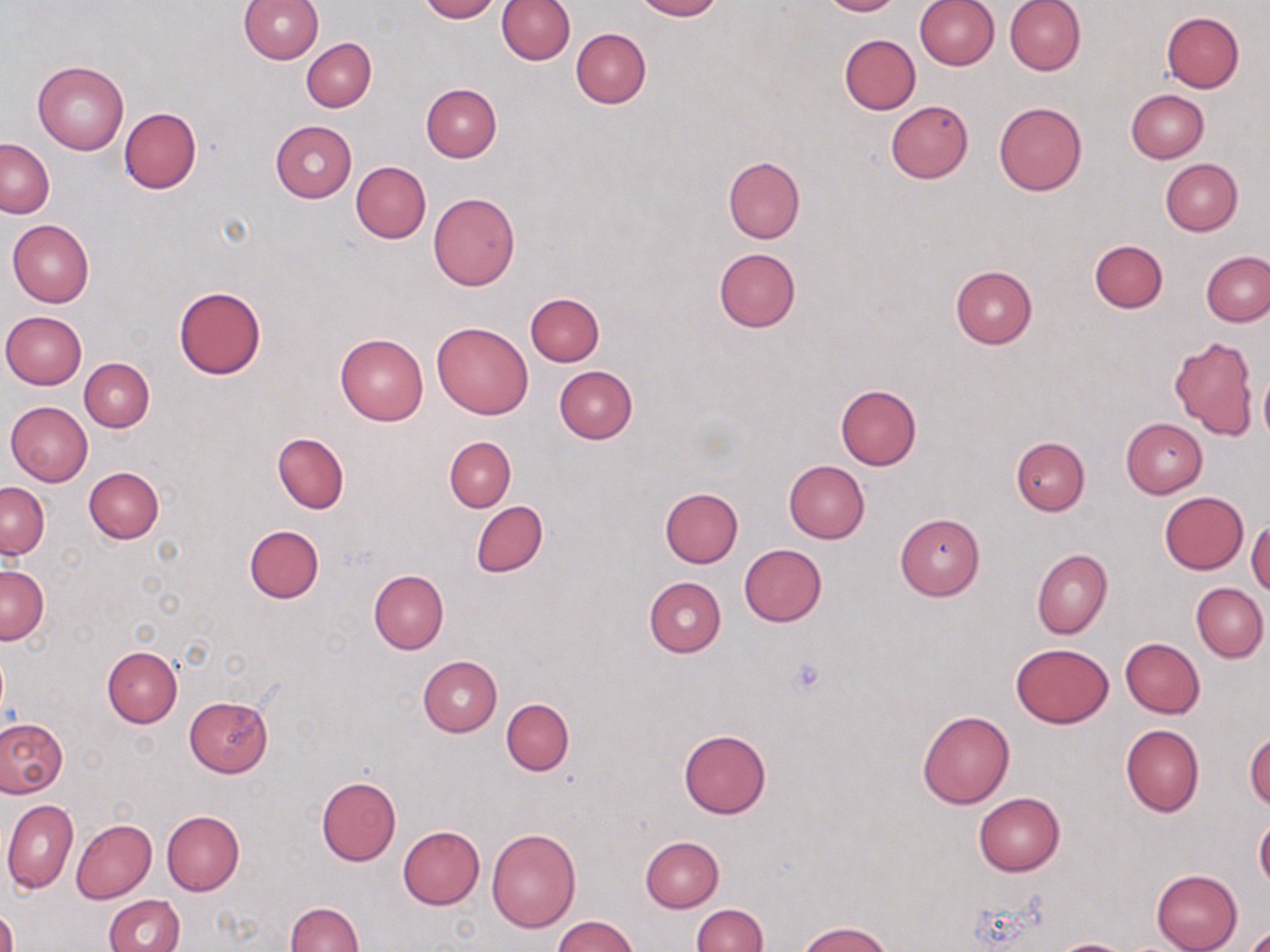
Approximate bounding boxes as (x1, y1, x2, y2) in pixels. Platelet locations: (786, 656, 830, 700). Uninfected red blood cell locations: (239, 0, 323, 63), (419, 0, 501, 22), (496, 0, 575, 65), (630, 0, 721, 20), (820, 0, 901, 15), (914, 0, 999, 71), (1005, 0, 1085, 75), (1162, 12, 1244, 92), (571, 28, 651, 108), (839, 34, 920, 114), (302, 38, 376, 112), (33, 60, 129, 154), (422, 84, 502, 162), (1126, 89, 1208, 162), (885, 101, 973, 183), (994, 101, 1087, 195), (119, 108, 201, 194), (270, 121, 357, 202), (1, 139, 54, 218), (723, 157, 805, 244), (1161, 158, 1243, 235), (351, 161, 431, 243), (429, 192, 520, 290), (8, 219, 94, 307), (1089, 240, 1167, 313), (714, 248, 800, 331), (1202, 253, 1270, 325), (951, 265, 1037, 348), (174, 286, 266, 379), (525, 293, 604, 366), (1, 310, 87, 388), (431, 321, 534, 420), (336, 333, 429, 424), (1169, 334, 1258, 439), (79, 357, 154, 431), (554, 366, 638, 443), (1258, 372, 1270, 446), (834, 383, 921, 469), (6, 401, 93, 485), (1121, 418, 1207, 497), (273, 432, 349, 513), (444, 436, 515, 511), (1012, 437, 1089, 515), (784, 461, 870, 543), (84, 467, 163, 543), (1, 481, 49, 558), (660, 487, 743, 567), (1159, 492, 1248, 574), (471, 501, 548, 576), (895, 513, 984, 600), (1247, 520, 1270, 595), (243, 525, 323, 603), (739, 543, 826, 626), (1031, 549, 1111, 638), (0, 566, 48, 644), (368, 570, 449, 654), (644, 576, 727, 657), (1191, 582, 1268, 662), (1121, 638, 1205, 718), (1010, 644, 1114, 728), (102, 647, 182, 727), (418, 655, 502, 737), (184, 696, 273, 776), (501, 698, 573, 775), (917, 711, 1014, 808), (0, 717, 69, 798), (1120, 724, 1204, 817), (678, 728, 772, 818), (1246, 730, 1269, 812), (316, 776, 401, 865), (974, 792, 1065, 876), (2, 799, 78, 894), (161, 811, 243, 895), (72, 819, 157, 902), (1255, 819, 1270, 893), (397, 826, 485, 910), (487, 828, 580, 932), (641, 836, 724, 912), (1150, 869, 1242, 952), (104, 894, 185, 952), (285, 901, 363, 952), (690, 904, 767, 952), (0, 906, 18, 952), (552, 915, 639, 952), (799, 922, 893, 952), (1246, 924, 1270, 951), (1050, 939, 1136, 952). Slide-level diagnosis: negative for blood parasites. 1000x magnification. May-Grünwald-Giemsa stain. Light microscopy. One field of a larger specimen. Image is 1270×952 pixels. Thin blood smear.